Outline each blood parasite and name the species.
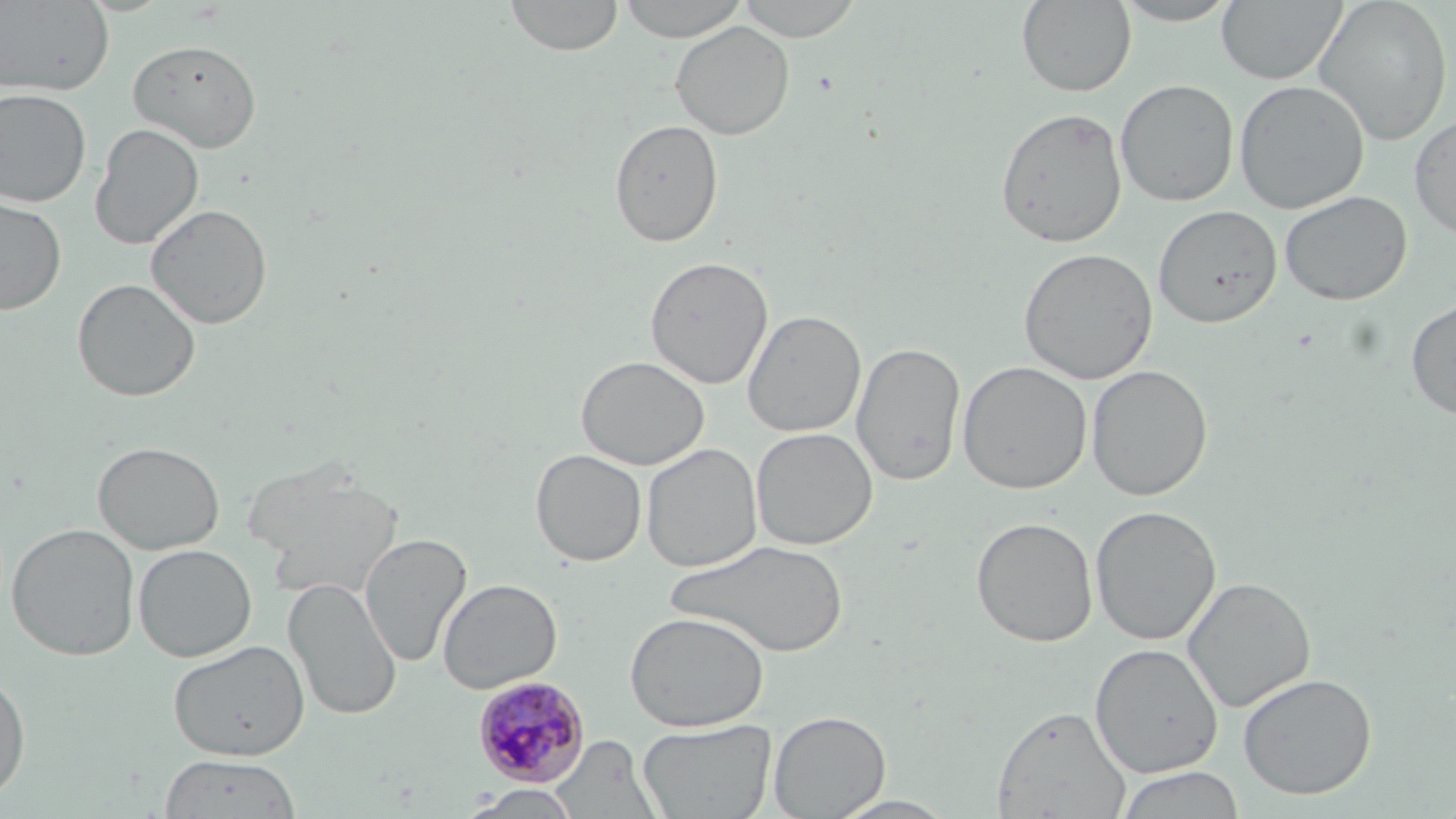
Approximate bounding boxes as (x1, y1, x2, y2) in pixels.
Plasmodium malariae-infected red blood cells: (471, 675, 591, 787).
No Plasmodium falciparum, Plasmodium ovale, Plasmodium vivax, Babesia divergens, or Trypanosoma brucei observed.

Uninfected red blood cell locations: (505, 0, 623, 57), (616, 0, 750, 42), (734, 0, 866, 41), (1217, 0, 1347, 85), (1313, 0, 1453, 146), (1, 1, 114, 97), (1016, 1, 1137, 96), (1112, 1, 1242, 26), (671, 21, 795, 140), (127, 38, 262, 152), (1115, 79, 1239, 206), (1233, 79, 1369, 214), (0, 88, 92, 207), (995, 107, 1128, 248), (1409, 112, 1456, 238), (609, 119, 724, 247), (89, 122, 205, 251), (1278, 190, 1412, 306), (0, 196, 67, 314), (145, 203, 273, 329), (1153, 205, 1281, 327), (1018, 247, 1157, 384), (644, 256, 773, 389), (72, 278, 201, 402), (1405, 296, 1456, 419), (743, 309, 866, 438), (852, 341, 966, 485), (576, 355, 710, 470), (957, 360, 1093, 494), (1086, 364, 1213, 501), (751, 427, 878, 550), (93, 441, 225, 554), (641, 443, 763, 573), (530, 448, 647, 566), (243, 459, 402, 600), (1089, 505, 1222, 646), (971, 516, 1098, 647), (7, 523, 139, 661), (359, 532, 471, 668), (665, 539, 850, 658), (133, 543, 257, 662), (1182, 576, 1316, 713), (284, 578, 402, 720), (437, 578, 562, 693), (625, 611, 770, 732), (168, 639, 309, 761), (1090, 643, 1223, 777), (0, 670, 31, 803), (1238, 672, 1377, 799), (991, 704, 1132, 819), (768, 710, 891, 818), (637, 719, 776, 818), (548, 735, 664, 819), (159, 754, 301, 818), (1113, 766, 1247, 819), (465, 785, 582, 818), (828, 794, 960, 819). Slide-level diagnosis: Plasmodium malariae. Light microscopy. May-Grünwald-Giemsa-stained preparation. One field of a larger specimen. Thin blood smear. Image is 1456×819 pixels. 1000x magnification.